Classify this cell by malaria status.
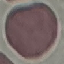

It is uninfected.

Thin smear of blood. Cell patch, automatically extracted from a larger field of view and resized to 64 × 64 pixels. Giemsa stain. Photographed with a smartphone camera at the microscope eyepiece.